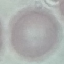
Summary:
  - Malaria status: uninfected
  - Stain: Giemsa
  - Preparation: thin blood smear
  - Capture: smartphone through the microscope eyepiece
  - Image type: automatically extracted cell patch, resized to 64 × 64 pixels